Locate every Plasmodium malariae-infected red blood cell.
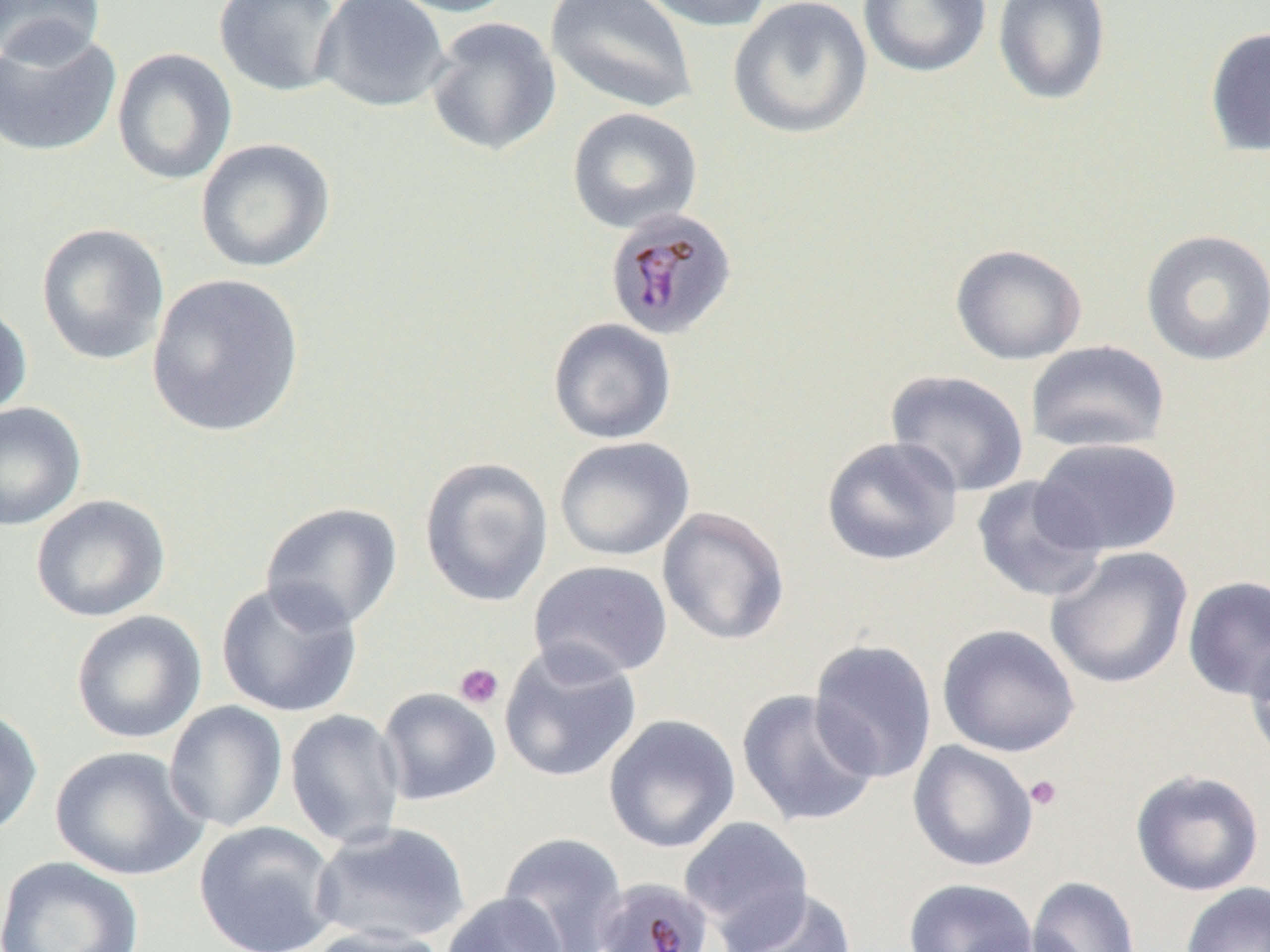
Approximate bounding boxes as [x1, y1, x2, y2] in pixels.
Plasmodium malariae-infected red blood cells: [603, 207, 738, 340].

slide_level_diagnosis: Plasmodium malariae
magnification: 1000x
uninfected_red_blood_cell_locations: 'approximate bounding boxes as [x1, y1, x2, y2] in pixels: [0, 0, 106, 65], [214, 0, 343, 98], [313, 0, 452, 113], [382, 0, 520, 18], [545, 0, 698, 115], [631, 0, 775, 33], [727, 0, 873, 140], [857, 0, 992, 78], [991, 0, 1112, 106], [425, 16, 562, 157], [0, 25, 123, 158], [1204, 25, 1270, 159], [112, 47, 237, 185], [567, 107, 703, 234], [195, 137, 336, 273], [36, 222, 170, 366], [1140, 228, 1270, 366], [950, 243, 1087, 365], [146, 273, 305, 438], [0, 299, 32, 422], [547, 318, 677, 445], [1025, 340, 1171, 454], [885, 369, 1030, 497], [0, 401, 86, 531], [821, 435, 963, 567], [554, 436, 695, 561], [1032, 438, 1183, 557], [419, 456, 554, 608], [971, 475, 1106, 603], [30, 494, 171, 622], [260, 502, 403, 632], [657, 505, 791, 646], [1045, 546, 1194, 690], [528, 560, 673, 682], [1182, 575, 1270, 701], [215, 579, 364, 718], [70, 610, 207, 744], [936, 623, 1081, 757], [1245, 638, 1270, 766], [808, 639, 938, 784], [499, 641, 642, 784], [377, 687, 502, 806], [735, 689, 880, 828], [163, 700, 288, 833], [0, 706, 43, 838], [284, 709, 406, 850], [603, 714, 741, 854], [907, 740, 1039, 872], [49, 745, 208, 882], [1129, 768, 1266, 897], [679, 816, 815, 947], [194, 820, 341, 952], [310, 822, 471, 947], [497, 831, 630, 952], [0, 855, 145, 951], [1026, 876, 1141, 952], [902, 878, 1038, 952], [1180, 882, 1270, 952], [721, 886, 858, 952], [440, 892, 568, 952], [301, 925, 453, 952]'
image_size: 1270×952 pixels
platelet_locations: 'approximate bounding boxes as [x1, y1, x2, y2] in pixels: [454, 663, 503, 709], [1025, 775, 1063, 811]'
preparation: thin blood smear
field_of_view: one of a larger specimen
modality: optical microscopy